State which parasite is depicted.
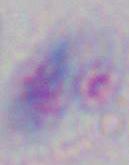
This is Toxoplasma gondii.

{
  "modality": "micrograph",
  "magnification": "1000x"
}